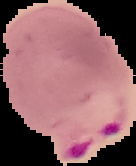

Image is 136×166 pixels. Malaria status: parasitized. From a thin blood smear. The area outside the segmented cell region is set to black.